Assess the morphology of the erythrocytes.
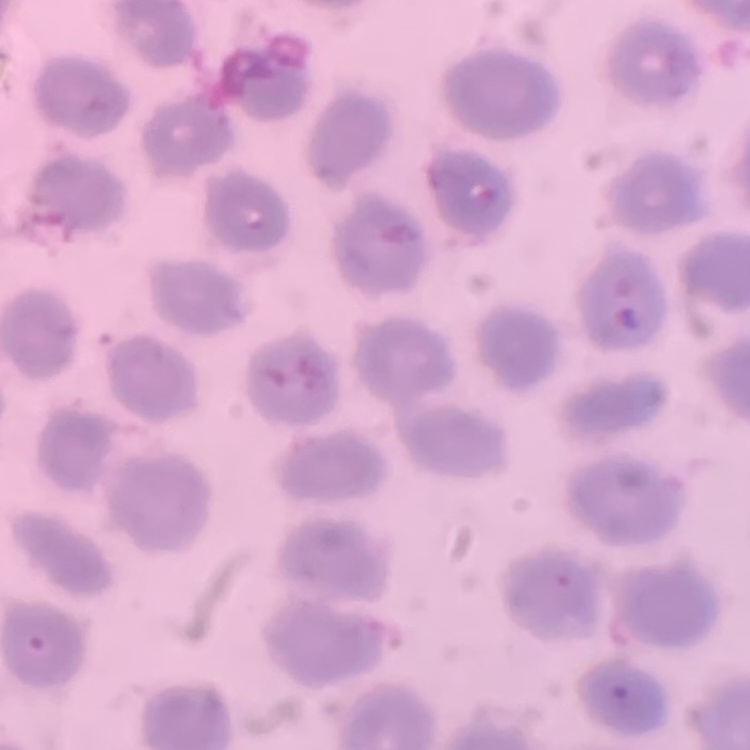
No rouleaux formation.

Thin peripheral smear. Stained with either Field's or Giemsa. One tile cut from a larger photomicrograph.